Outline each uninfected red blood cell.
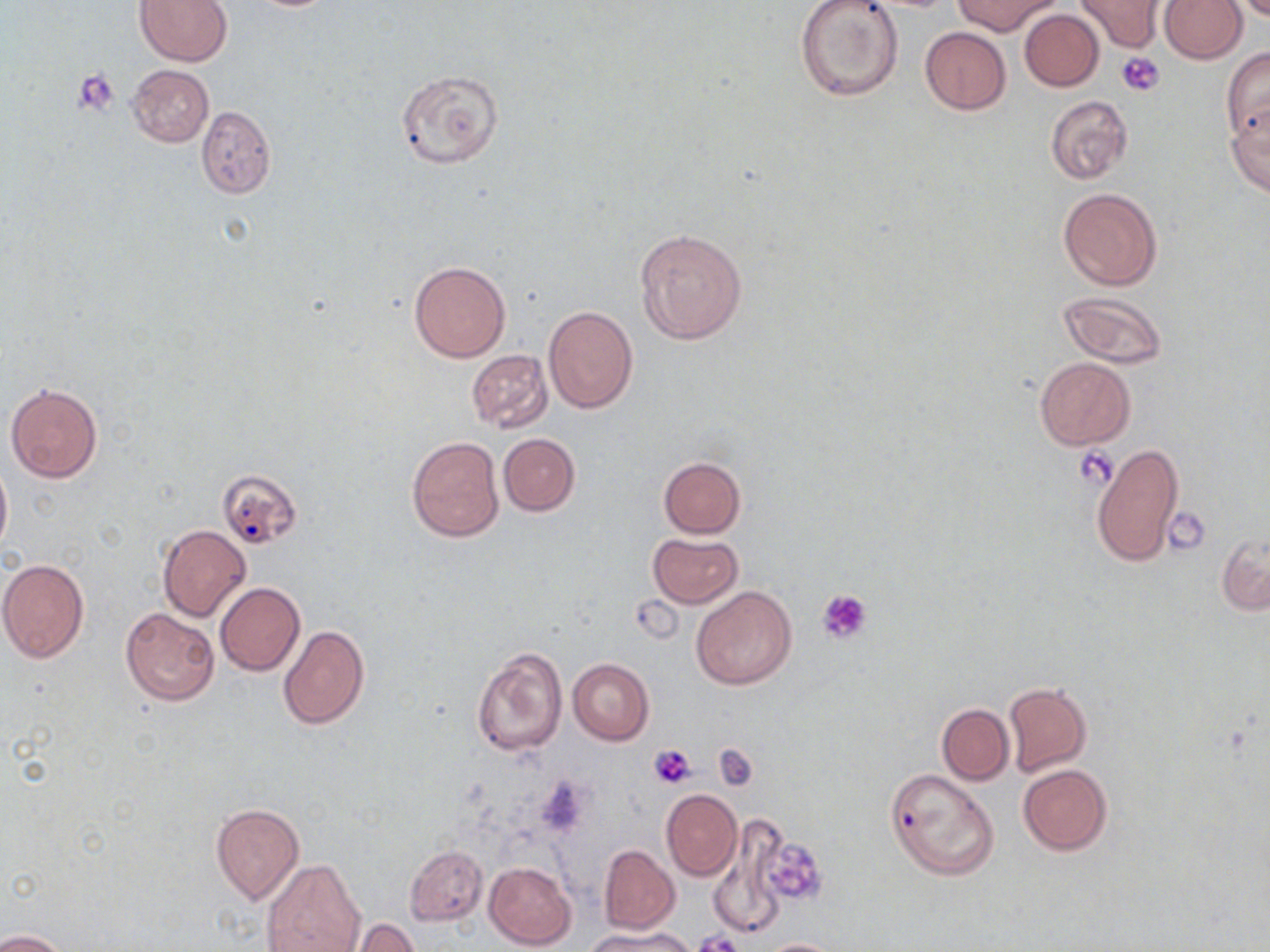

Approximate bounding boxes as (x1, y1, x2, y2) in pixels.
Uninfected red blood cells: (134, 0, 234, 67), (792, 0, 904, 103), (954, 0, 1059, 35), (1159, 0, 1246, 64), (1072, 1, 1165, 53), (1019, 9, 1104, 91), (920, 26, 1011, 115), (1221, 48, 1270, 142), (127, 65, 213, 147), (396, 69, 505, 170), (1045, 95, 1133, 184), (1227, 104, 1270, 198), (195, 105, 275, 199), (1058, 188, 1161, 291), (634, 228, 748, 344), (408, 262, 511, 362), (1057, 289, 1168, 370), (543, 305, 639, 414), (465, 349, 554, 434), (1034, 357, 1135, 449), (5, 382, 103, 483), (498, 433, 579, 516), (406, 436, 504, 540), (1089, 441, 1184, 569), (0, 455, 12, 559), (658, 456, 746, 538), (216, 468, 302, 549), (158, 525, 250, 620), (647, 532, 743, 608), (1215, 533, 1269, 615), (0, 558, 89, 663), (215, 582, 305, 676), (692, 585, 797, 690), (121, 608, 218, 706), (278, 624, 369, 730), (469, 645, 566, 758), (568, 658, 654, 746), (1003, 681, 1093, 777), (937, 703, 1014, 784), (1018, 764, 1112, 855), (885, 768, 1000, 879), (661, 789, 742, 881), (210, 803, 304, 904), (708, 817, 791, 936), (747, 820, 830, 918), (405, 845, 487, 926), (600, 845, 678, 933), (260, 858, 365, 951), (484, 860, 578, 950), (347, 918, 422, 952), (586, 926, 699, 952), (1, 929, 71, 952), (761, 938, 844, 952).

Summary:
  - Platelet locations: (1117, 51, 1165, 95), (74, 69, 119, 116), (1074, 445, 1119, 489), (1168, 512, 1206, 552), (817, 589, 873, 645), (713, 744, 756, 789), (649, 745, 696, 788), (753, 833, 830, 910), (693, 932, 743, 952)
  - Slide-level diagnosis: negative for blood parasites
  - Stain: May-Grünwald-Giemsa
  - Magnification: 1000x
  - Image size: 1270×952 pixels
  - Field of view: single
  - Preparation: thin blood smear
  - Modality: optical microscopy